Assess this cell for malaria.
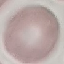

Uninfected.

Summary:
  - Preparation: thin blood smear
  - Image type: automatically extracted cell patch, resized to 64 × 64 pixels
  - Capture: smartphone camera at the microscope eyepiece
  - Stain: Giemsa